Draw a bounding box around every malaria parasite, every leukocyte, and every artifact (stain precipitate or debris).
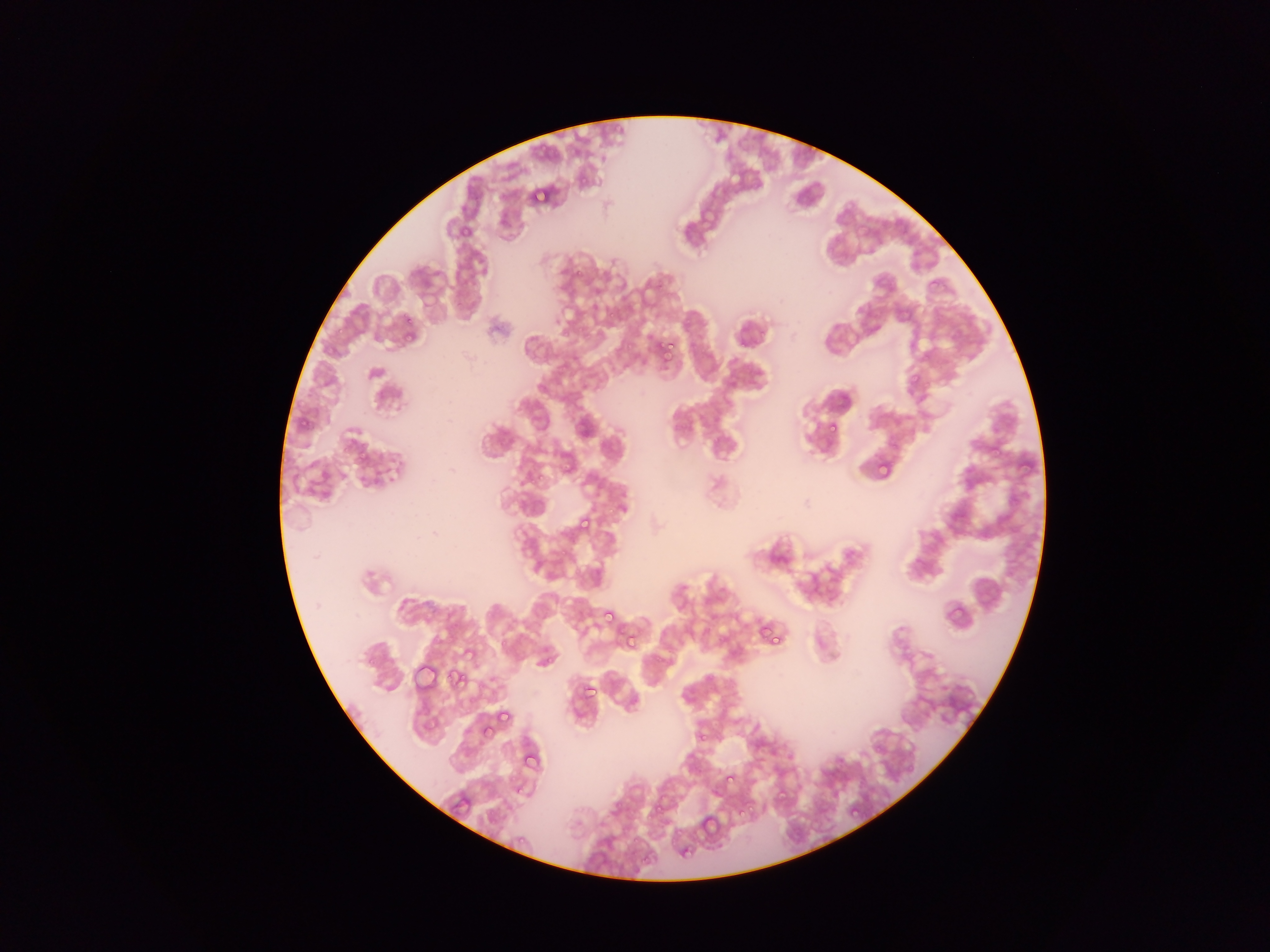

Approximate bounding boxes as [left, top, right, bottom] in pixels.
Malaria parasites: [528, 186, 550, 208], [458, 224, 468, 243], [571, 265, 588, 281], [927, 275, 945, 293], [644, 279, 664, 300], [608, 306, 619, 319], [400, 311, 417, 332], [560, 330, 572, 340], [625, 336, 639, 355], [664, 338, 675, 350], [660, 347, 676, 360], [906, 370, 924, 391], [827, 421, 839, 433], [990, 439, 1007, 457], [872, 444, 903, 486], [1015, 453, 1036, 476], [875, 455, 896, 479], [525, 468, 546, 491], [575, 515, 594, 536], [943, 601, 966, 626], [601, 606, 618, 624], [756, 621, 782, 648], [621, 630, 640, 653], [498, 632, 517, 652], [448, 667, 469, 691], [580, 681, 597, 700], [497, 710, 512, 726], [477, 730, 502, 741], [697, 730, 710, 743], [520, 747, 543, 772], [724, 776, 739, 789], [825, 785, 842, 802], [772, 786, 791, 808], [513, 788, 526, 796], [648, 800, 668, 823], [847, 802, 862, 819], [735, 804, 756, 821], [697, 811, 723, 841], [517, 835, 528, 846], [675, 841, 697, 862].
No leukocytes observed.

{
  "capture": "mobile-phone photograph through a microscope",
  "field_of_view": "single",
  "preparation": "thin blood film",
  "country": "Ghana",
  "image_size": "1270×952 pixels"
}